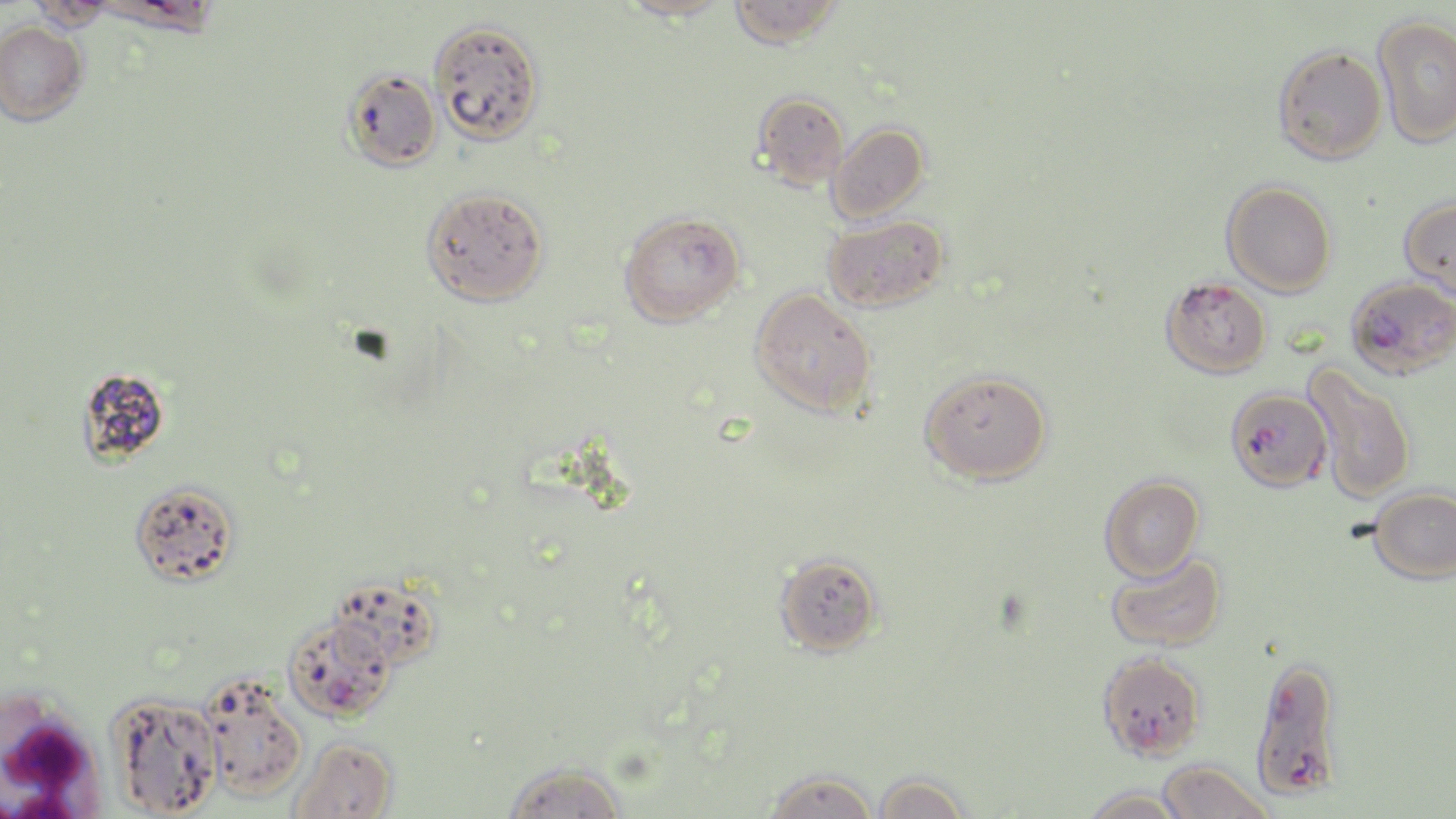

Approximate bounding boxes as (x1,y1)-(x2,y2) corner pairs in pixels. Uninfected red blood cell locations: (617,0)-(730,22), (729,0)-(842,49), (26,1)-(117,33), (1372,14)-(1456,149), (430,19)-(545,146), (0,20)-(88,125), (1272,44)-(1387,164), (341,68)-(442,173), (753,91)-(850,190), (826,122)-(929,224), (1221,180)-(1337,297), (421,186)-(549,306), (1399,196)-(1456,299), (618,210)-(745,327), (822,214)-(949,313), (1161,276)-(1272,378), (749,287)-(876,418), (1303,363)-(1417,503), (75,365)-(172,467), (919,369)-(1053,485), (1099,474)-(1205,581), (129,480)-(240,588), (1368,485)-(1456,584), (773,551)-(883,657), (1105,551)-(1227,652), (330,573)-(444,673), (1096,651)-(1206,762), (198,673)-(307,802), (106,691)-(223,817), (287,737)-(399,819), (1156,758)-(1276,819), (501,761)-(629,819), (763,769)-(880,819), (871,771)-(972,819), (1079,788)-(1191,819). Plasmodium falciparum-infected red blood cell locations: (1346,277)-(1456,379), (1224,387)-(1332,493), (282,613)-(397,723), (1249,655)-(1345,801). White blood cell locations: (0,698)-(102,815). Slide-level diagnosis: Plasmodium falciparum. Single field of view. Thin blood film. Image is 1456×819 pixels. Optical microscopy. May-Grünwald-Giemsa stain. Captured at 1000x magnification.